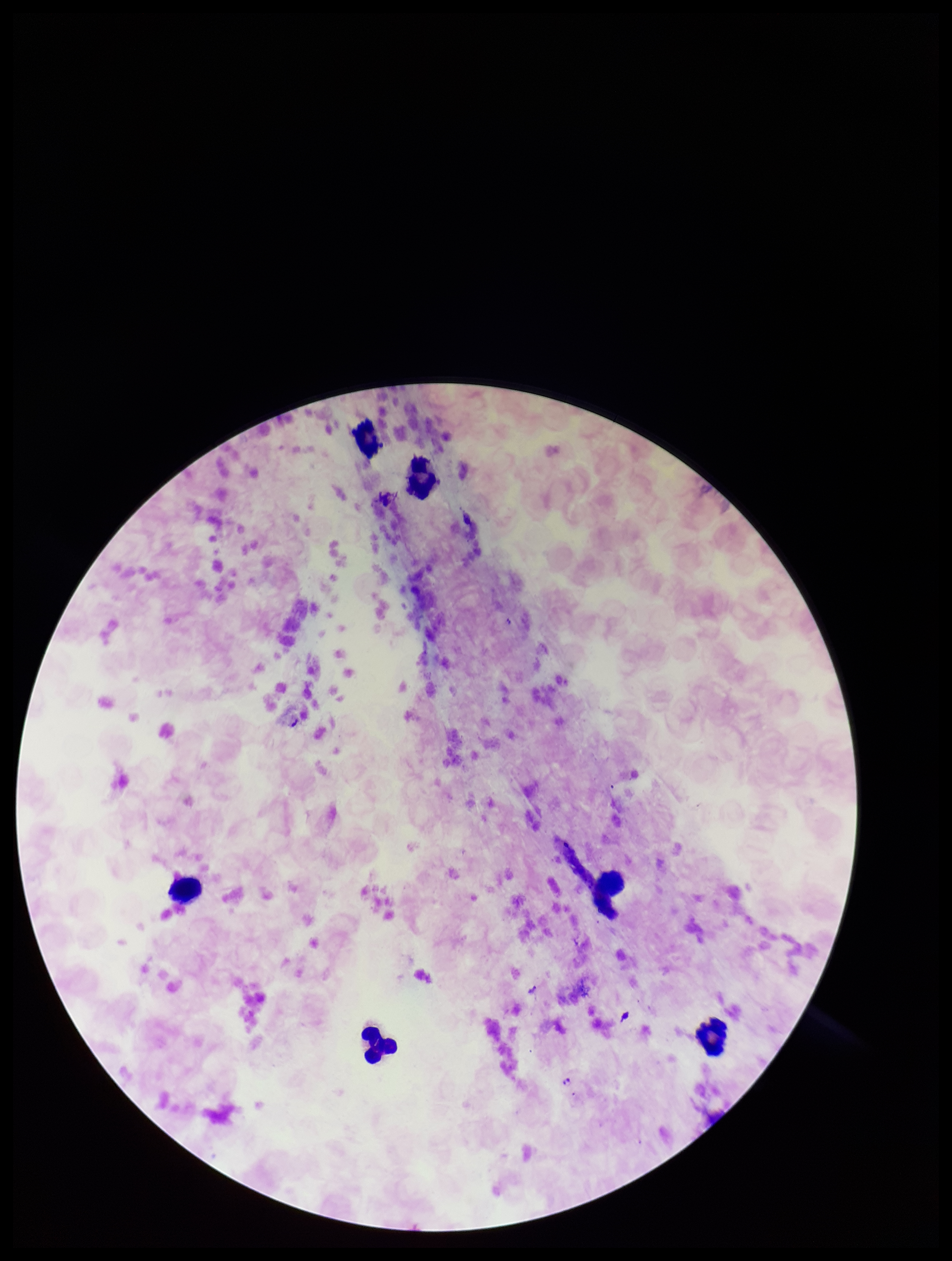
Giemsa stain. Image is 952×1261 pixels. Parasite count: 0. Preparation: thick blood smear. Photographed through the microscope eyepiece with a smartphone camera. Plasmodium parasites: none identified. Species reported for this patient: Plasmodium falciparum. Leukocyte count: 6. Patient malaria status: infected. Single field of view.